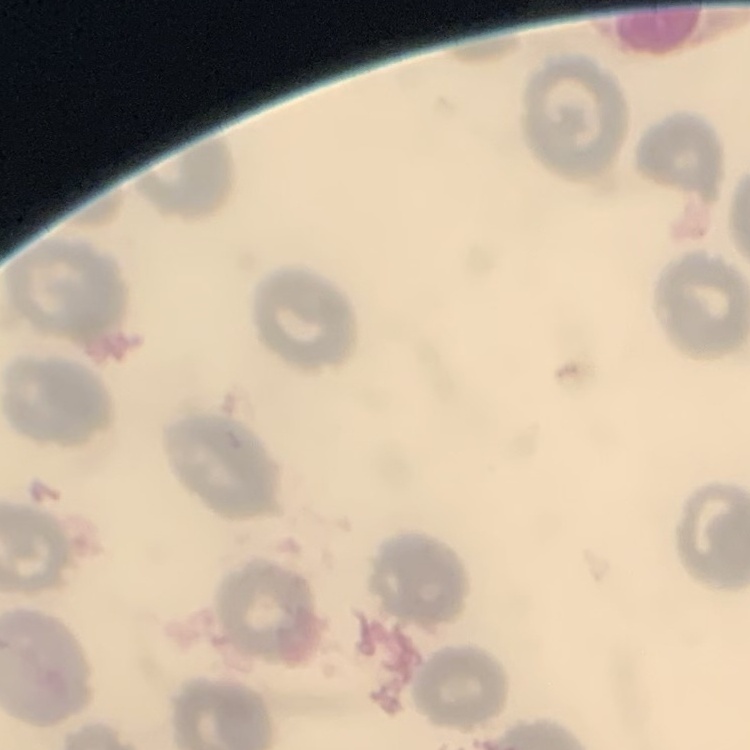

Summary:
  - Red blood cell morphology: no rouleaux formation
  - Image type: one tile cut from a larger photomicrograph
  - Preparation: thin blood film
  - Stain: Field's or Giemsa